Locate every malaria parasite.
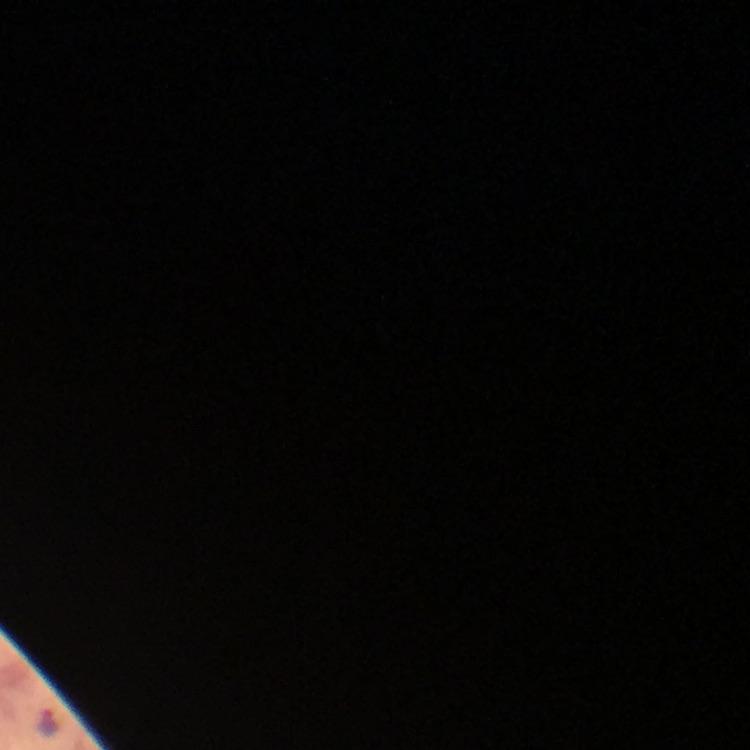

Approximate centers as [x, y] in pixels.
Malaria parasites: [49, 724].

stain = Giemsa
immersion oil = used
cropped from = one field of view
preparation = thick smear
magnification = 100x
context = from a malaria diagnostic workup
image size = 750×750 pixels
capture = smartphone camera through the microscope